Evaluate for malaria.
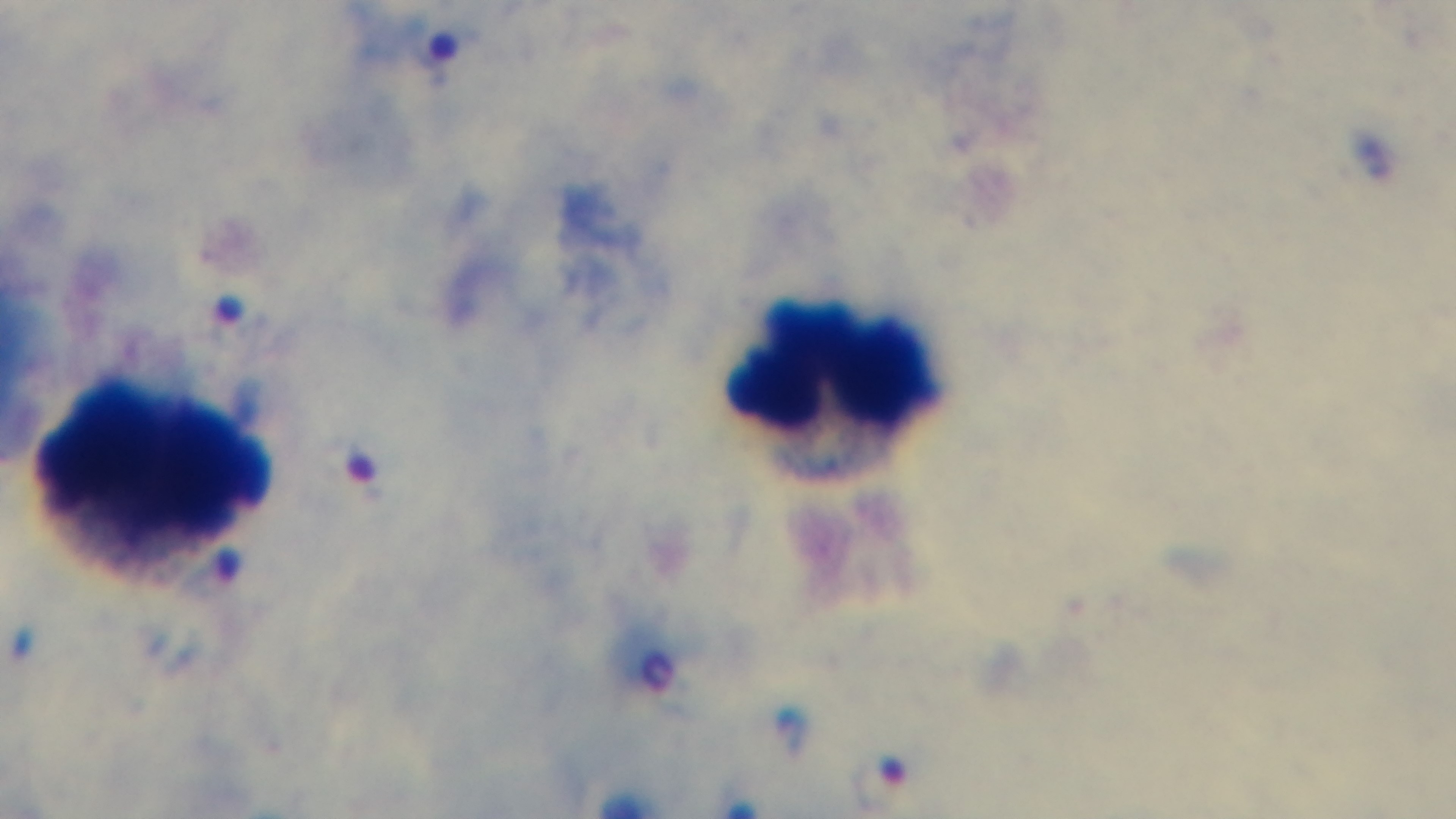
Positive.

field of view = one from the slide
stain = Giemsa
objective = 100x oil immersion
preparation = thick blood film
capture = mounted 4K digital camera
modality = light microscopy